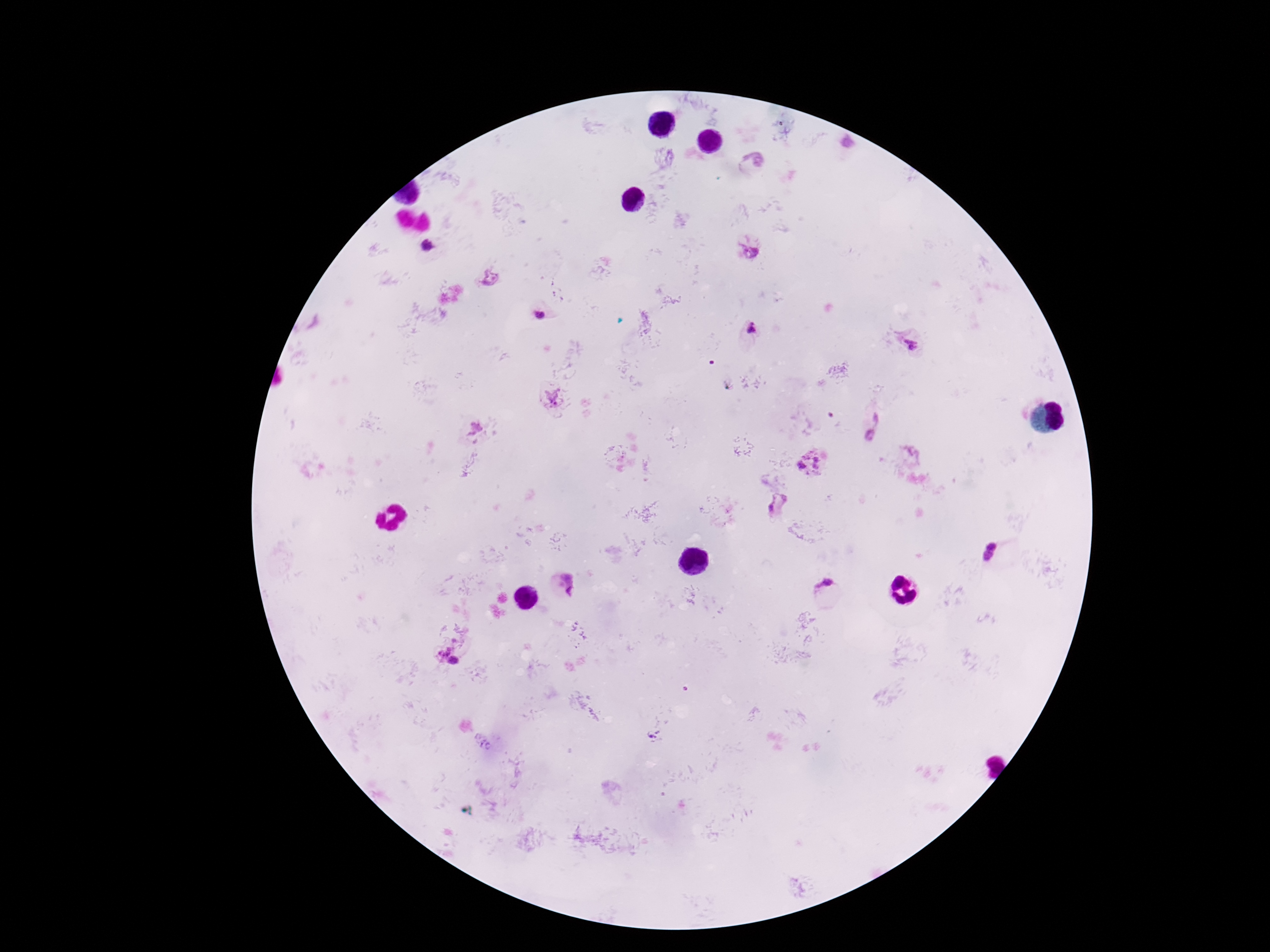

Approximate centers as {x, y} in pixels. Plasmodium parasite locations: {847, 144}, {755, 162}, {425, 246}, {751, 253}, {490, 277}, {540, 315}, {752, 327}, {912, 345}, {554, 397}, {876, 420}, {474, 428}, {869, 434}, {806, 453}, {816, 459}, {802, 465}, {816, 467}, {777, 504}, {992, 546}, {987, 555}, {569, 586}, {825, 588}, {443, 649}, {454, 661}. Image is 1270×952 pixels. Patient malaria status: positive. Giemsa stain. 100x magnification. Thick blood film. One field from this slide. Photographed through the microscope eyepiece with a smartphone camera.